Give the position of every Plasmodium parasite visible.
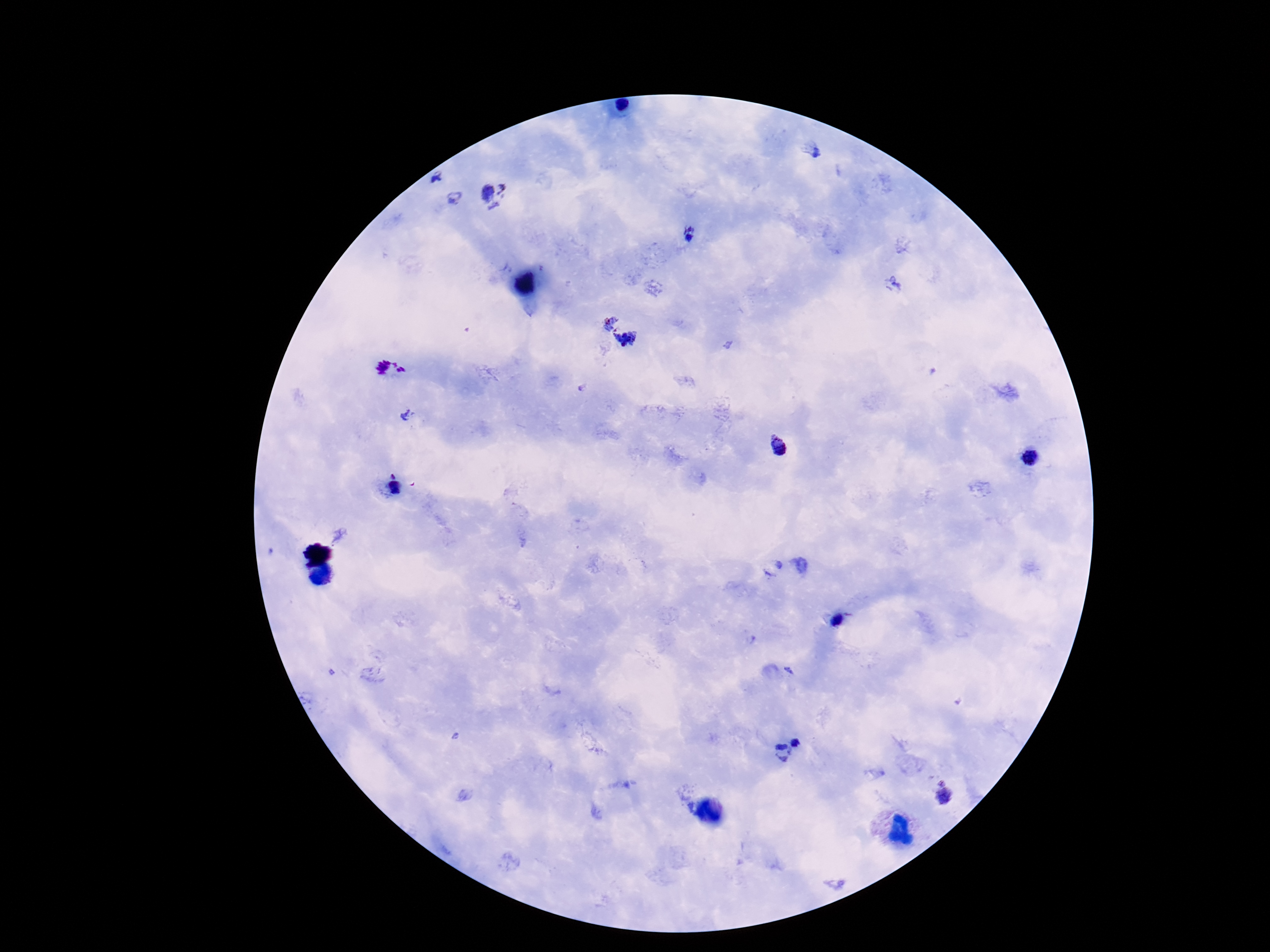
Approximate centers as (x, y) in pixels.
Plasmodium parasites: (815, 152), (438, 178), (495, 194), (455, 198), (689, 236), (894, 285), (606, 321), (630, 342), (391, 370), (409, 414), (781, 451), (1032, 457), (394, 485), (837, 621), (796, 740), (781, 752), (941, 782), (945, 796).

stain = Giemsa
capture = smartphone camera through the microscope eyepiece
preparation = thick blood film
patient malaria status = positive
magnification = 100x
image size = 1270×952 pixels
field of view = single